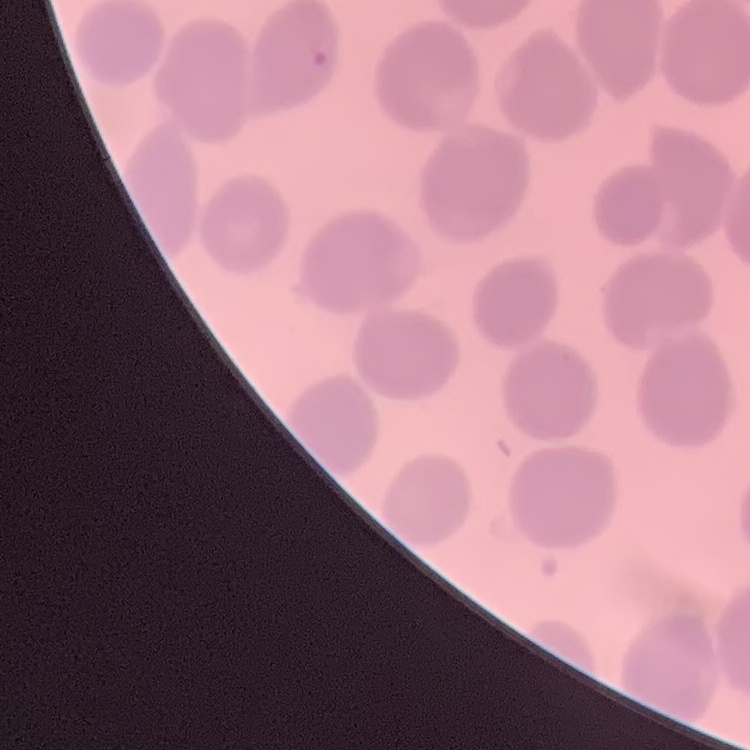
The red blood cells exhibit no rouleaux formation. Square crop of a larger photomicrograph. Thin blood smear. Stained with either Field's or Giemsa.